Outline each Plasmodium vivax-infected red blood cell.
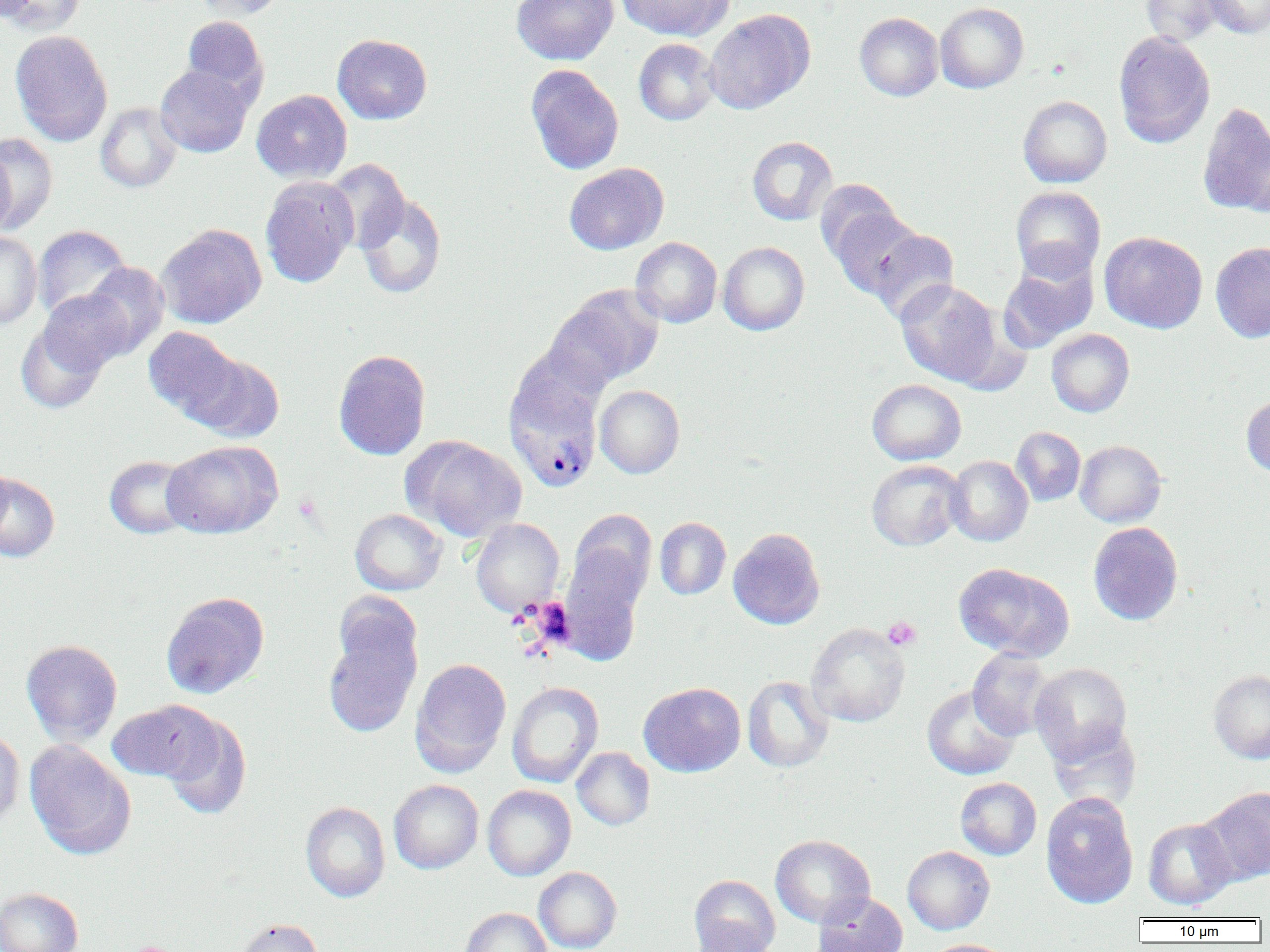
Approximate bounding boxes as [x1, y1, x2, y2] in pixels.
Plasmodium vivax-infected red blood cells: [505, 383, 601, 492].

Summary:
  - Uninfected red blood cell locations: [1, 0, 86, 35], [192, 0, 289, 20], [512, 0, 618, 65], [615, 0, 733, 40], [1141, 0, 1225, 46], [1202, 0, 1270, 37], [935, 2, 1029, 93], [704, 9, 815, 114], [854, 12, 943, 101], [180, 16, 267, 101], [10, 30, 113, 147], [1113, 31, 1215, 148], [332, 34, 432, 124], [634, 38, 720, 125], [156, 64, 253, 157], [525, 65, 624, 175], [252, 90, 352, 183], [1018, 95, 1112, 187], [95, 102, 182, 193], [1197, 102, 1270, 216], [1, 133, 58, 232], [747, 136, 837, 225], [0, 147, 17, 239], [325, 159, 410, 254], [564, 162, 669, 254], [259, 176, 359, 289], [814, 179, 902, 265], [1011, 186, 1106, 281], [355, 192, 447, 298], [828, 205, 924, 299], [155, 224, 267, 329], [33, 225, 131, 322], [868, 228, 960, 324], [1100, 231, 1207, 333], [0, 232, 42, 330], [631, 237, 722, 328], [1210, 241, 1270, 343], [718, 242, 809, 335], [998, 251, 1099, 352], [80, 262, 170, 357], [895, 280, 1003, 386], [548, 286, 664, 389], [37, 289, 133, 376], [16, 322, 108, 414], [144, 326, 243, 421], [1046, 329, 1134, 417], [509, 346, 607, 432], [333, 349, 431, 461], [185, 351, 285, 443], [867, 379, 966, 465], [595, 385, 684, 478], [1241, 393, 1270, 477], [1011, 427, 1085, 506], [404, 435, 526, 542], [161, 440, 283, 539], [1075, 440, 1167, 527], [104, 455, 197, 539], [945, 456, 1033, 546], [0, 460, 14, 547], [866, 460, 965, 551], [0, 472, 60, 563], [350, 508, 447, 595], [654, 517, 731, 600], [470, 518, 565, 616], [1087, 522, 1184, 625], [728, 528, 825, 629], [558, 540, 650, 665], [953, 562, 1074, 661], [161, 591, 269, 698], [322, 600, 423, 738], [806, 623, 910, 727], [21, 639, 123, 745], [968, 648, 1055, 740], [410, 658, 512, 775], [1029, 663, 1133, 764], [1209, 670, 1270, 764], [742, 676, 833, 772], [507, 682, 603, 788], [639, 682, 745, 777], [922, 685, 1020, 780], [106, 700, 219, 785], [157, 711, 252, 820], [1047, 720, 1142, 813], [0, 728, 25, 831], [25, 739, 136, 860], [572, 747, 655, 830], [955, 777, 1041, 860], [389, 779, 483, 874], [483, 785, 576, 880], [1197, 786, 1270, 885], [1040, 793, 1138, 909], [301, 801, 390, 902], [1143, 818, 1237, 910], [770, 834, 876, 928], [902, 846, 994, 935], [534, 867, 621, 952], [689, 874, 781, 952], [0, 887, 83, 952], [813, 893, 907, 952], [459, 907, 552, 952], [234, 918, 324, 952], [689, 921, 777, 952], [924, 939, 1016, 952]
  - Platelet locations: [883, 617, 921, 651], [124, 941, 179, 952]
  - Slide-level diagnosis: Plasmodium vivax
  - Field of view: one of a larger specimen
  - Modality: light microscopy
  - Image size: 1270×952 pixels
  - Magnification: 1000x
  - Preparation: thin blood film